Describe the morphology of the erythrocytes.
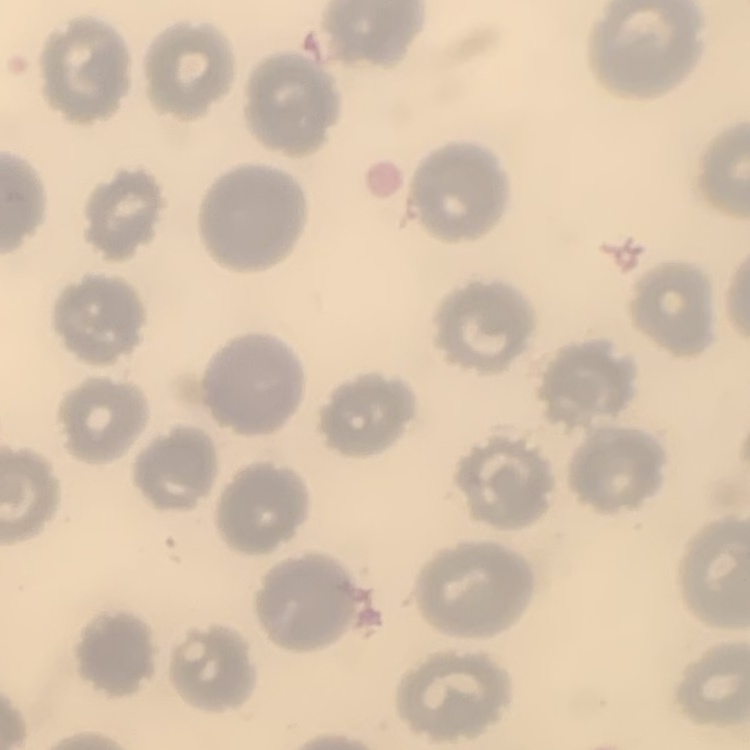

They show no rouleaux formation.

image_type: square crop of a larger photomicrograph
preparation: thin blood film
stain: Field's or Giemsa